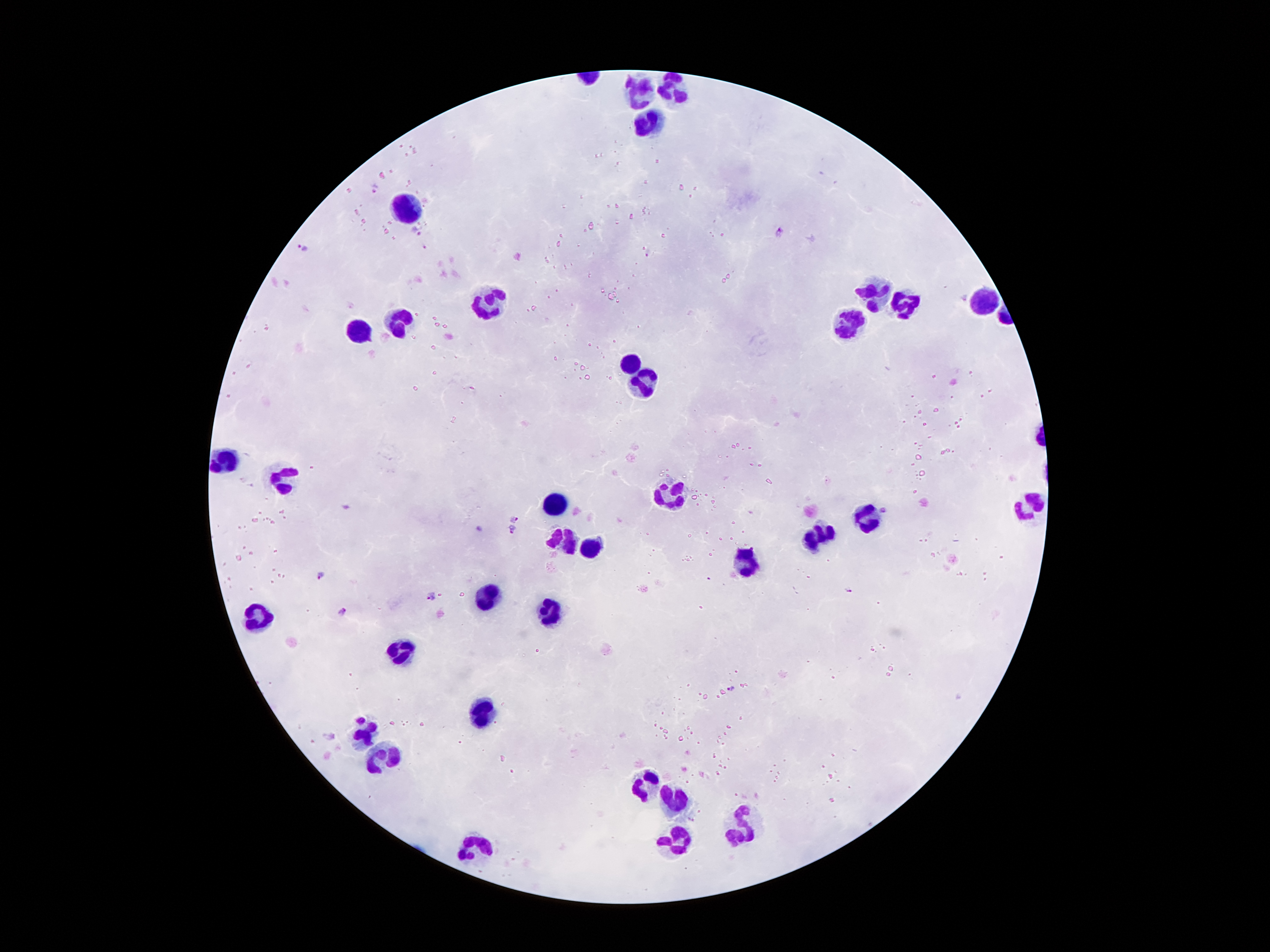 Approximate centers as [x, y] in pixels. Leukocyte locations: [677, 86], [641, 88], [643, 118], [404, 204], [984, 296], [900, 300], [490, 302], [843, 321], [393, 323], [358, 327], [631, 357], [645, 380], [225, 458], [282, 477], [666, 491], [551, 500], [1032, 502], [868, 512], [822, 533], [557, 535], [585, 546], [742, 560], [486, 592], [257, 611], [553, 613], [398, 647], [480, 712], [366, 737], [383, 752], [648, 787], [671, 804], [740, 823], [673, 842], [471, 844]. Plasmodium parasite locations: [374, 188], [417, 231], [780, 233], [302, 249], [884, 511], [515, 518], [479, 528], [511, 531], [321, 574], [849, 589], [432, 595], [342, 611], [730, 688], [362, 719], [329, 734]. Thick blood smear. Giemsa-stained preparation. One field from this slide. Smartphone photograph taken through the microscope eyepiece. 100x magnification. Patient malaria status: infected with Plasmodium falciparum. Image is 1270×952 pixels.